Report the malaria status of this cell.
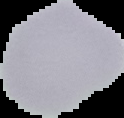

Uninfected.

Summary:
  - Image size: 124×118 pixels
  - Image type: segmented cell region with the area outside set to black
  - Preparation: thin blood smear